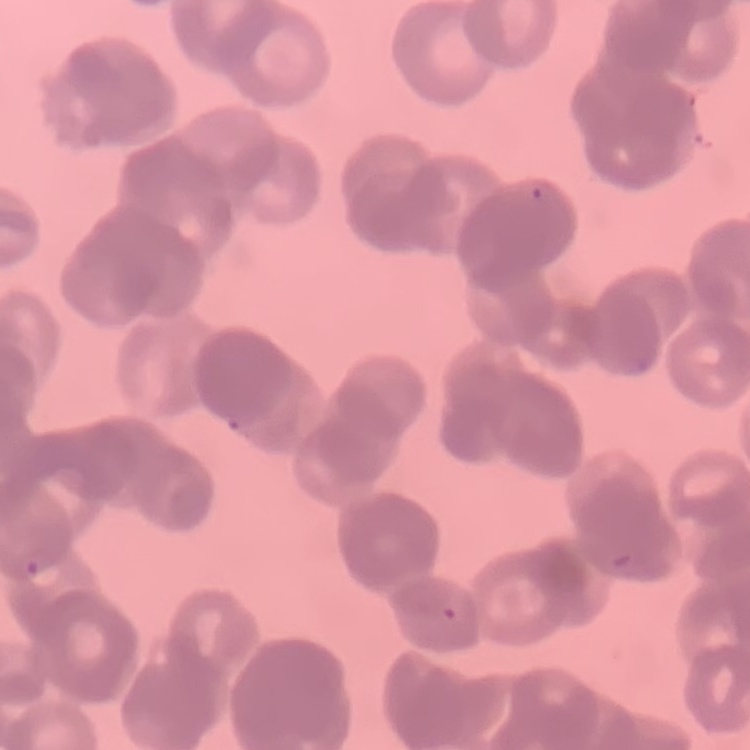 The erythrocytes show rouleaux formation. Field's or Giemsa stain. Square crop of a larger photomicrograph. Thin blood smear.